Outline each Plasmodium vivax-infected red blood cell.
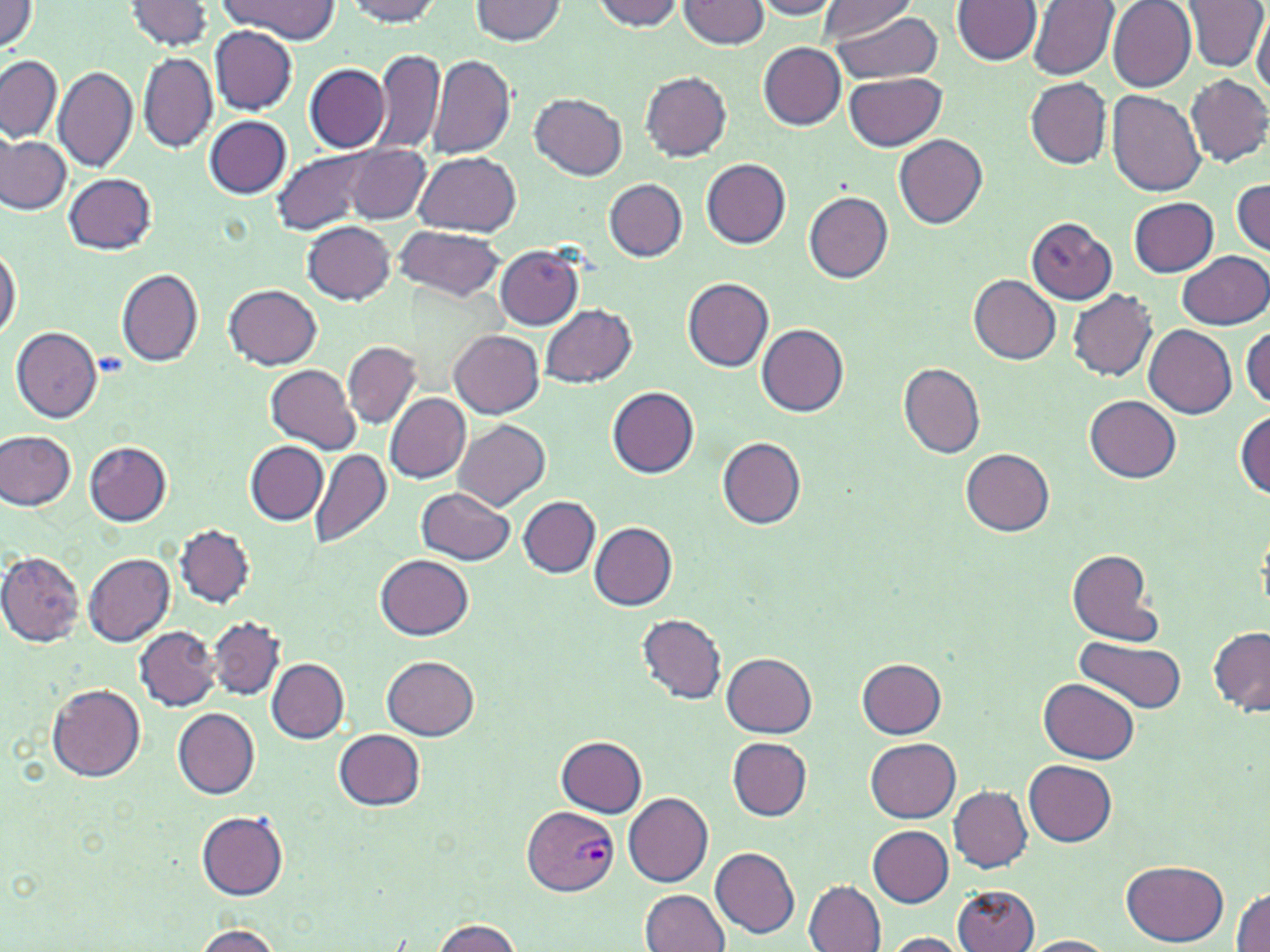
Approximate bounding boxes as named x1/y1/x2/y2 corners in pixels.
Plasmodium vivax-infected red blood cells: (x1=522, y1=804, x2=620, y2=897).

slide-level diagnosis = Plasmodium vivax
preparation = thin blood film
image size = 1270×952 pixels
stain = May-Grünwald-Giemsa
uninfected red blood cell locations = approximate bounding boxes as named x1/y1/x2/y2 corners in pixels: (x1=217, y1=0, x2=340, y2=41), (x1=343, y1=0, x2=445, y2=25), (x1=468, y1=0, x2=568, y2=45), (x1=750, y1=0, x2=842, y2=19), (x1=817, y1=0, x2=921, y2=42), (x1=952, y1=0, x2=1040, y2=66), (x1=125, y1=1, x2=215, y2=52), (x1=590, y1=1, x2=688, y2=32), (x1=679, y1=1, x2=769, y2=49), (x1=1027, y1=1, x2=1118, y2=80), (x1=1107, y1=1, x2=1195, y2=92), (x1=1186, y1=1, x2=1269, y2=72), (x1=0, y1=2, x2=43, y2=55), (x1=824, y1=9, x2=947, y2=82), (x1=1251, y1=9, x2=1269, y2=98), (x1=209, y1=25, x2=297, y2=113), (x1=758, y1=43, x2=847, y2=130), (x1=370, y1=47, x2=447, y2=158), (x1=427, y1=52, x2=517, y2=161), (x1=139, y1=53, x2=215, y2=152), (x1=0, y1=55, x2=62, y2=143), (x1=304, y1=63, x2=390, y2=153), (x1=54, y1=65, x2=137, y2=172), (x1=641, y1=70, x2=732, y2=161), (x1=845, y1=73, x2=946, y2=151), (x1=1185, y1=74, x2=1270, y2=168), (x1=1026, y1=78, x2=1112, y2=168), (x1=1106, y1=91, x2=1205, y2=196), (x1=531, y1=92, x2=626, y2=180), (x1=205, y1=115, x2=290, y2=198), (x1=895, y1=134, x2=987, y2=228), (x1=0, y1=136, x2=71, y2=215), (x1=346, y1=145, x2=431, y2=225), (x1=272, y1=148, x2=386, y2=236), (x1=414, y1=154, x2=522, y2=235), (x1=702, y1=158, x2=790, y2=248), (x1=65, y1=172, x2=157, y2=253), (x1=604, y1=178, x2=687, y2=261), (x1=1231, y1=179, x2=1269, y2=255), (x1=803, y1=190, x2=893, y2=283), (x1=1129, y1=198, x2=1217, y2=276), (x1=1025, y1=217, x2=1117, y2=304), (x1=303, y1=221, x2=396, y2=304), (x1=394, y1=225, x2=506, y2=301), (x1=0, y1=241, x2=22, y2=344), (x1=495, y1=245, x2=585, y2=329), (x1=1177, y1=250, x2=1270, y2=329), (x1=115, y1=268, x2=205, y2=367), (x1=970, y1=275, x2=1061, y2=363), (x1=682, y1=277, x2=774, y2=371), (x1=225, y1=285, x2=321, y2=369), (x1=1068, y1=289, x2=1158, y2=382), (x1=541, y1=304, x2=638, y2=388), (x1=758, y1=324, x2=849, y2=416), (x1=1144, y1=325, x2=1237, y2=418), (x1=1242, y1=325, x2=1270, y2=412), (x1=11, y1=326, x2=103, y2=422), (x1=449, y1=330, x2=544, y2=418), (x1=342, y1=341, x2=421, y2=429), (x1=898, y1=361, x2=986, y2=458), (x1=266, y1=364, x2=361, y2=453), (x1=608, y1=386, x2=699, y2=477), (x1=385, y1=393, x2=470, y2=482), (x1=1084, y1=395, x2=1181, y2=482), (x1=1234, y1=410, x2=1269, y2=498), (x1=453, y1=419, x2=550, y2=512), (x1=0, y1=430, x2=75, y2=510), (x1=716, y1=437, x2=806, y2=529), (x1=84, y1=441, x2=172, y2=526), (x1=247, y1=441, x2=328, y2=524), (x1=961, y1=448, x2=1054, y2=535), (x1=310, y1=450, x2=392, y2=548), (x1=418, y1=488, x2=516, y2=564), (x1=519, y1=497, x2=600, y2=578), (x1=589, y1=522, x2=676, y2=609), (x1=177, y1=525, x2=255, y2=608), (x1=1066, y1=549, x2=1164, y2=646), (x1=0, y1=551, x2=85, y2=646), (x1=82, y1=553, x2=176, y2=647), (x1=377, y1=554, x2=474, y2=639), (x1=638, y1=614, x2=728, y2=704), (x1=209, y1=616, x2=285, y2=700), (x1=135, y1=625, x2=218, y2=710), (x1=1207, y1=628, x2=1270, y2=717), (x1=1076, y1=636, x2=1185, y2=713), (x1=721, y1=652, x2=817, y2=736), (x1=382, y1=657, x2=479, y2=741), (x1=267, y1=658, x2=349, y2=743), (x1=856, y1=659, x2=947, y2=738), (x1=1038, y1=679, x2=1139, y2=764), (x1=47, y1=683, x2=146, y2=781), (x1=173, y1=709, x2=259, y2=798), (x1=333, y1=729, x2=426, y2=810), (x1=556, y1=735, x2=647, y2=817), (x1=727, y1=738, x2=812, y2=820), (x1=866, y1=738, x2=961, y2=822), (x1=1024, y1=759, x2=1117, y2=845), (x1=949, y1=787, x2=1032, y2=872), (x1=624, y1=791, x2=714, y2=886), (x1=197, y1=812, x2=290, y2=901), (x1=868, y1=825, x2=953, y2=907), (x1=710, y1=847, x2=800, y2=938), (x1=1121, y1=859, x2=1229, y2=946), (x1=805, y1=880, x2=885, y2=952), (x1=953, y1=886, x2=1039, y2=952), (x1=1232, y1=888, x2=1270, y2=952), (x1=641, y1=890, x2=730, y2=952), (x1=428, y1=918, x2=525, y2=952), (x1=191, y1=924, x2=283, y2=951), (x1=878, y1=931, x2=973, y2=951), (x1=1019, y1=935, x2=1118, y2=952)
field of view = one of a larger specimen
magnification = 1000x
modality = optical microscopy